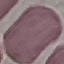

Summary:
  - Malaria status: uninfected
  - Capture: smartphone camera at the microscope eyepiece
  - Stain: Giemsa
  - Image type: automatically extracted cell patch, resized to 64 × 64 pixels
  - Preparation: thin blood smear